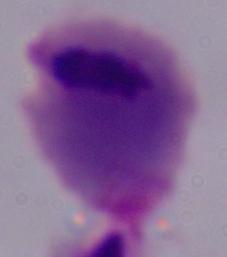 A trichomonad is shown. Micrograph. 1000x magnification.